Report the malaria status of this cell.
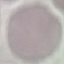
Uninfected.

Thin smear of blood. Giemsa-stained preparation. Cell patch, automatically extracted from a larger field of view and resized to 64 × 64 pixels. Acquired by smartphone through the microscope eyepiece.